State which parasite is depicted.
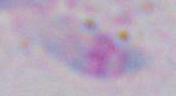

Toxoplasma gondii.

1000x magnification. Micrograph.